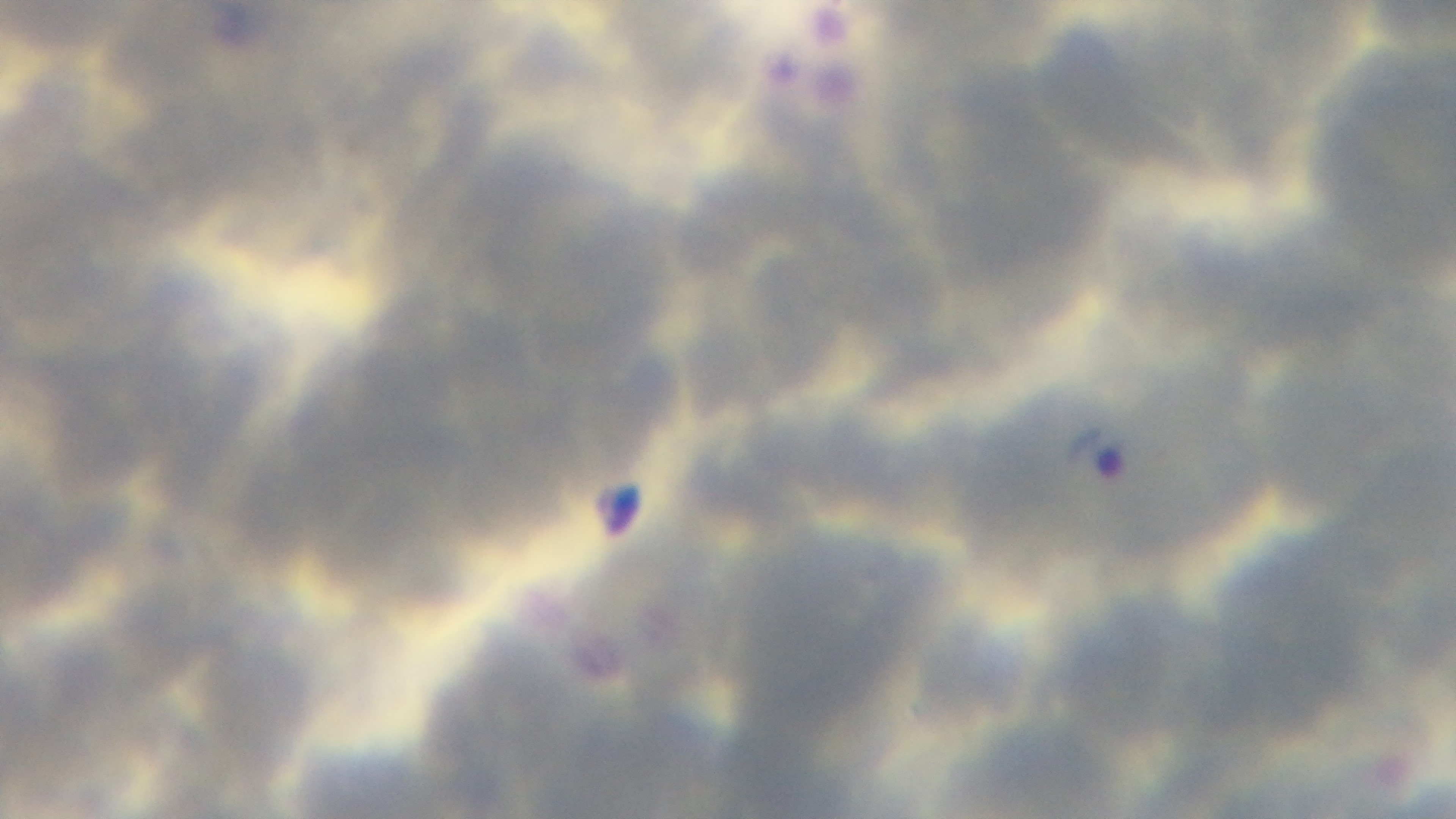

malaria status = infected
objective = 100x oil immersion
preparation = thin
capture = mounted 4K digital camera
modality = light microscopy
stain = Giemsa
field of view = single